State which parasite is depicted.
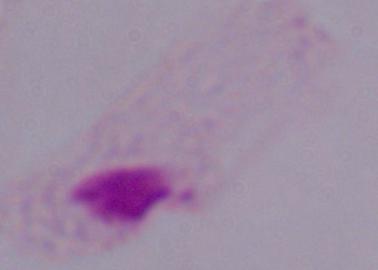
This is a trichomonad.

modality: photomicrograph
magnification: 1000x